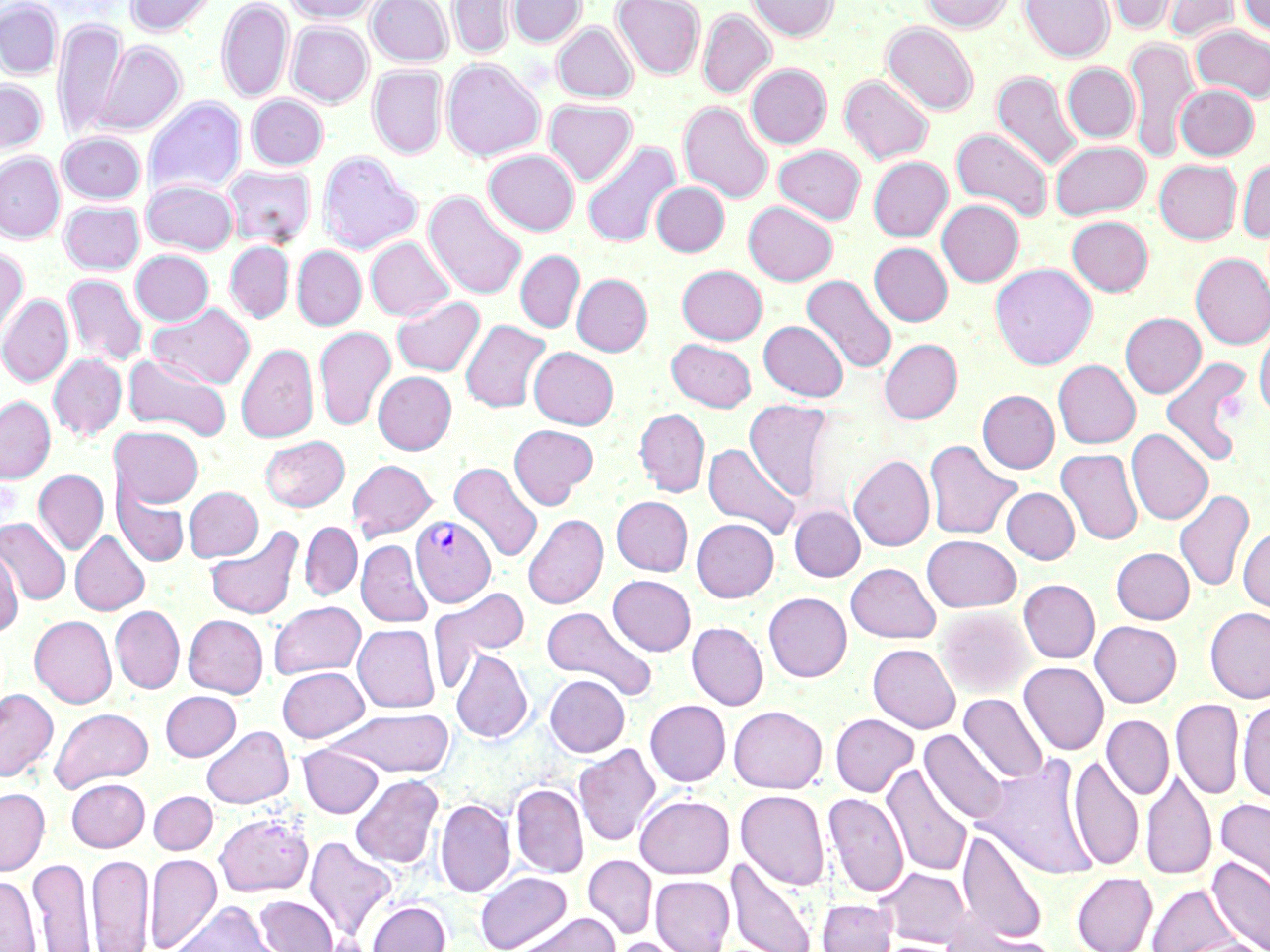
Summary:
  - Coordinate format: approximate bounding boxes as (x1,y1)-(x2,y2) corner pairs in pixels
  - Uninfected red blood cell locations: (126,0)-(217,36), (217,0)-(293,103), (285,0)-(378,24), (367,0)-(453,65), (448,0)-(515,59), (508,0)-(586,47), (612,0)-(705,80), (747,0)-(839,41), (922,0)-(1014,32), (1020,0)-(1114,62), (1100,0)-(1180,35), (1160,0)-(1241,43), (1238,0)-(1270,36), (0,1)-(62,79), (698,9)-(776,98), (53,18)-(125,142), (287,22)-(372,107), (552,22)-(637,102), (882,22)-(978,115), (1190,25)-(1270,102), (1124,37)-(1199,161), (93,39)-(185,136), (442,58)-(545,161), (1063,63)-(1139,142), (745,64)-(831,148), (368,66)-(448,158), (991,70)-(1083,172), (839,75)-(934,164), (0,80)-(47,156), (1174,84)-(1259,160), (247,95)-(328,169), (144,97)-(246,198), (544,99)-(637,185), (678,101)-(774,204), (951,128)-(1053,221), (58,132)-(145,204), (1050,141)-(1151,220), (582,142)-(680,248), (774,145)-(865,224), (484,149)-(579,235), (318,151)-(421,255), (0,153)-(64,243), (868,156)-(953,241), (1237,158)-(1270,242), (1154,159)-(1242,244), (223,165)-(316,247), (142,180)-(239,255), (651,182)-(729,257), (424,191)-(527,300), (936,198)-(1024,287), (60,201)-(144,274), (744,201)-(837,285), (1066,216)-(1153,296), (366,237)-(455,321), (226,241)-(293,323), (869,242)-(953,326), (292,246)-(366,330), (0,247)-(28,345), (130,250)-(214,326), (515,250)-(585,333), (1191,253)-(1270,349), (990,263)-(1097,369), (677,265)-(767,344), (572,273)-(652,356), (63,274)-(147,367), (801,274)-(897,374), (0,294)-(73,387), (391,296)-(484,376), (147,302)-(255,390), (1120,312)-(1205,398), (461,319)-(550,413), (758,321)-(848,401), (1254,324)-(1270,418), (314,326)-(396,431), (666,338)-(756,411), (879,339)-(962,424), (236,343)-(318,443), (529,347)-(618,429), (123,352)-(232,442), (48,353)-(126,441), (1161,355)-(1253,467), (1053,359)-(1140,448), (373,371)-(456,454), (977,390)-(1059,474), (0,396)-(55,483), (744,399)-(833,501), (634,408)-(710,497), (508,423)-(598,509), (110,425)-(204,508), (1126,428)-(1213,524), (260,435)-(349,512), (923,438)-(1022,541), (703,442)-(801,539), (1056,448)-(1142,545), (849,454)-(935,551), (347,459)-(437,540), (449,462)-(542,563), (33,469)-(108,555), (114,484)-(189,567), (184,486)-(263,561), (1002,487)-(1079,563), (1174,489)-(1254,592), (611,496)-(693,575), (789,505)-(865,581), (523,514)-(607,609), (0,518)-(71,605), (692,518)-(779,602), (299,522)-(362,600), (205,525)-(304,621), (1237,525)-(1270,615), (70,531)-(150,615), (921,534)-(1021,612), (356,539)-(432,627), (0,547)-(23,636), (1111,547)-(1194,623), (846,562)-(941,643), (608,575)-(696,655), (1018,579)-(1100,663), (430,587)-(529,686), (763,592)-(852,681), (268,601)-(366,678), (110,605)-(184,693), (542,606)-(657,701), (936,606)-(1033,698), (1204,607)-(1270,703), (180,610)-(366,689), (183,614)-(268,697), (29,615)-(116,707), (1090,621)-(1182,707), (687,622)-(768,709), (353,624)-(439,712), (868,643)-(961,733), (450,649)-(533,743), (1019,661)-(1109,755), (277,666)-(369,742), (545,674)-(629,757), (0,688)-(58,781), (160,690)-(241,761), (959,693)-(1048,784), (1171,698)-(1244,799), (1237,699)-(1270,804), (645,700)-(731,786), (728,705)-(827,793), (50,707)-(153,791), (326,707)-(454,777), (830,713)-(919,797), (1102,714)-(1174,799), (202,725)-(294,808), (920,729)-(1008,825), (574,743)-(660,847), (298,744)-(383,817), (1068,755)-(1144,871), (977,757)-(1098,879), (882,763)-(974,878), (1141,767)-(1217,881), (350,774)-(443,868), (66,778)-(149,851), (511,783)-(589,878), (0,788)-(50,875), (735,790)-(830,890), (149,791)-(217,854), (823,792)-(908,897), (634,794)-(735,879), (1215,797)-(1270,901), (435,798)-(515,897), (214,812)-(314,897), (957,828)-(1048,946), (303,836)-(399,942), (87,853)-(154,952), (145,853)-(222,952), (582,854)-(657,939), (1207,855)-(1270,952), (27,856)-(95,952), (726,856)-(817,952), (877,867)-(972,947), (474,871)-(572,951), (1072,872)-(1157,952), (0,875)-(41,952), (651,875)-(735,952), (1147,882)-(1241,952), (254,895)-(338,952), (817,898)-(897,952), (367,900)-(450,952), (169,901)-(283,952), (512,912)-(622,952), (941,917)-(1050,952), (610,936)-(699,952), (1175,938)-(1270,952)
  - Plasmodium vivax-infected red blood cell locations: (410,515)-(496,608)
  - Slide-level diagnosis: Plasmodium vivax
  - Image size: 1270×952 pixels
  - Stain: May-Grünwald-Giemsa
  - Modality: optical microscopy
  - Field of view: one of a larger specimen
  - Magnification: 1000x
  - Preparation: thin blood smear